Describe the morphology of the erythrocytes.
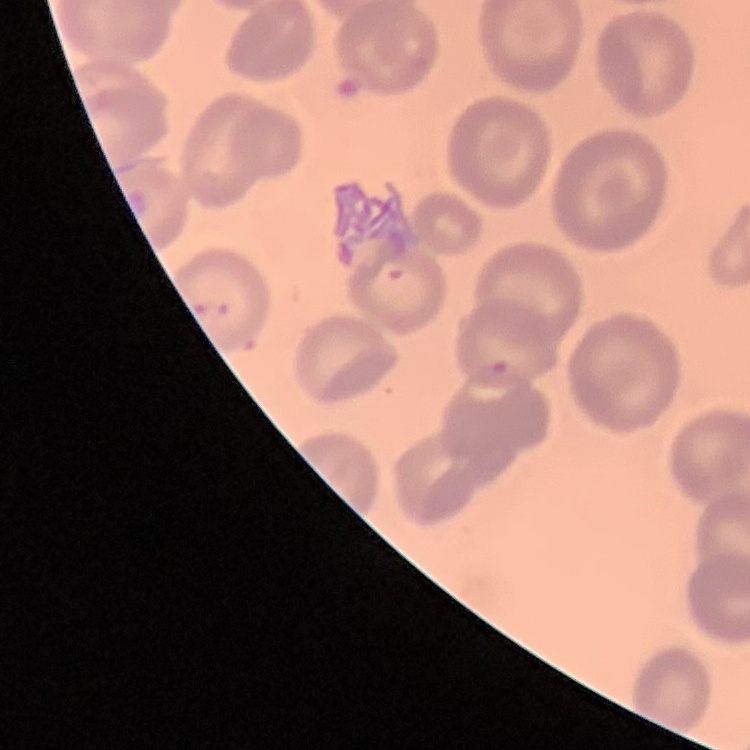
They show no rouleaux formation.

Summary:
  - Image type: one tile cut from a larger photomicrograph
  - Stain: Field's or Giemsa
  - Preparation: thin blood film